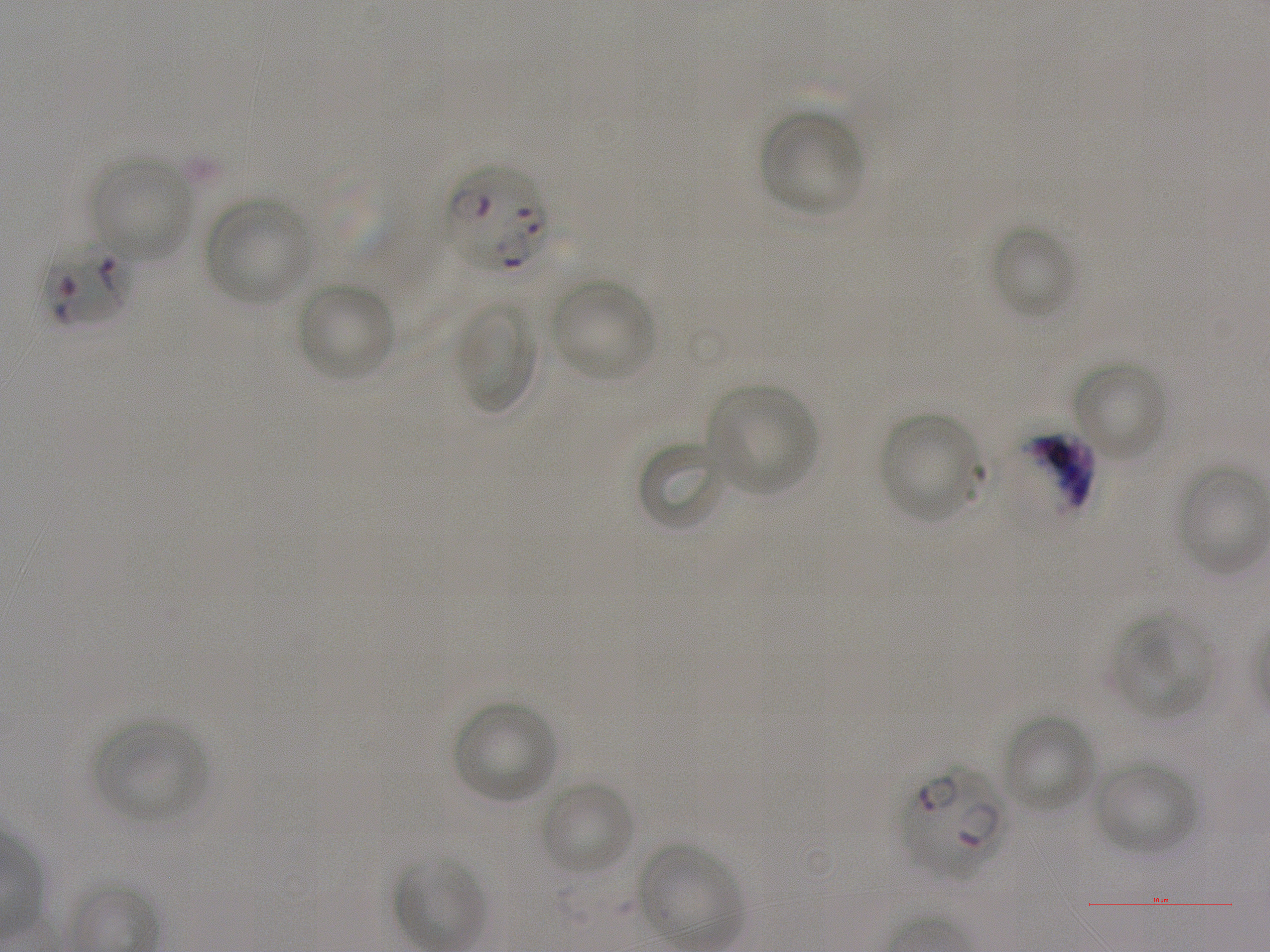

Not every red blood cell is marked.
{
  "locations_of_uninfected_red_blood_cells": "approximate bounding boxes as {x1, y1, x2, y2} in pixels: {759, 110, 865, 218}, {89, 156, 195, 262}, {205, 196, 314, 307}, {989, 224, 1077, 319}, {550, 278, 656, 383}, {295, 280, 396, 383}, {454, 301, 537, 415}, {1073, 361, 1167, 461}, {707, 384, 818, 496}, {879, 412, 985, 525}, {637, 439, 728, 533}, {1112, 614, 1212, 718}, {453, 701, 557, 805}, {1000, 714, 1098, 813}, {92, 719, 208, 823}, {1091, 758, 1200, 857}, {539, 781, 634, 876}",
  "objective": "100x, oil immersion, numerical aperture 1.25",
  "locations_of_infected_red_blood_cells": "approximate bounding boxes as {x1, y1, x2, y2} in pixels: {447, 162, 550, 275}, {41, 238, 136, 330}, {901, 765, 1008, 879}",
  "field_of_view": "single",
  "locations_of_red_blood_cells_of_indeterminate_infection_status": "approximate bounding boxes as {x1, y1, x2, y2} in pixels: {999, 429, 1095, 532}",
  "donor_blood_group": "A+",
  "preparation": "thin blood film",
  "stain": "Giemsa",
  "image_size": "1270×952 pixels",
  "culture": "in-vitro P. falciparum strain NF54, static"
}